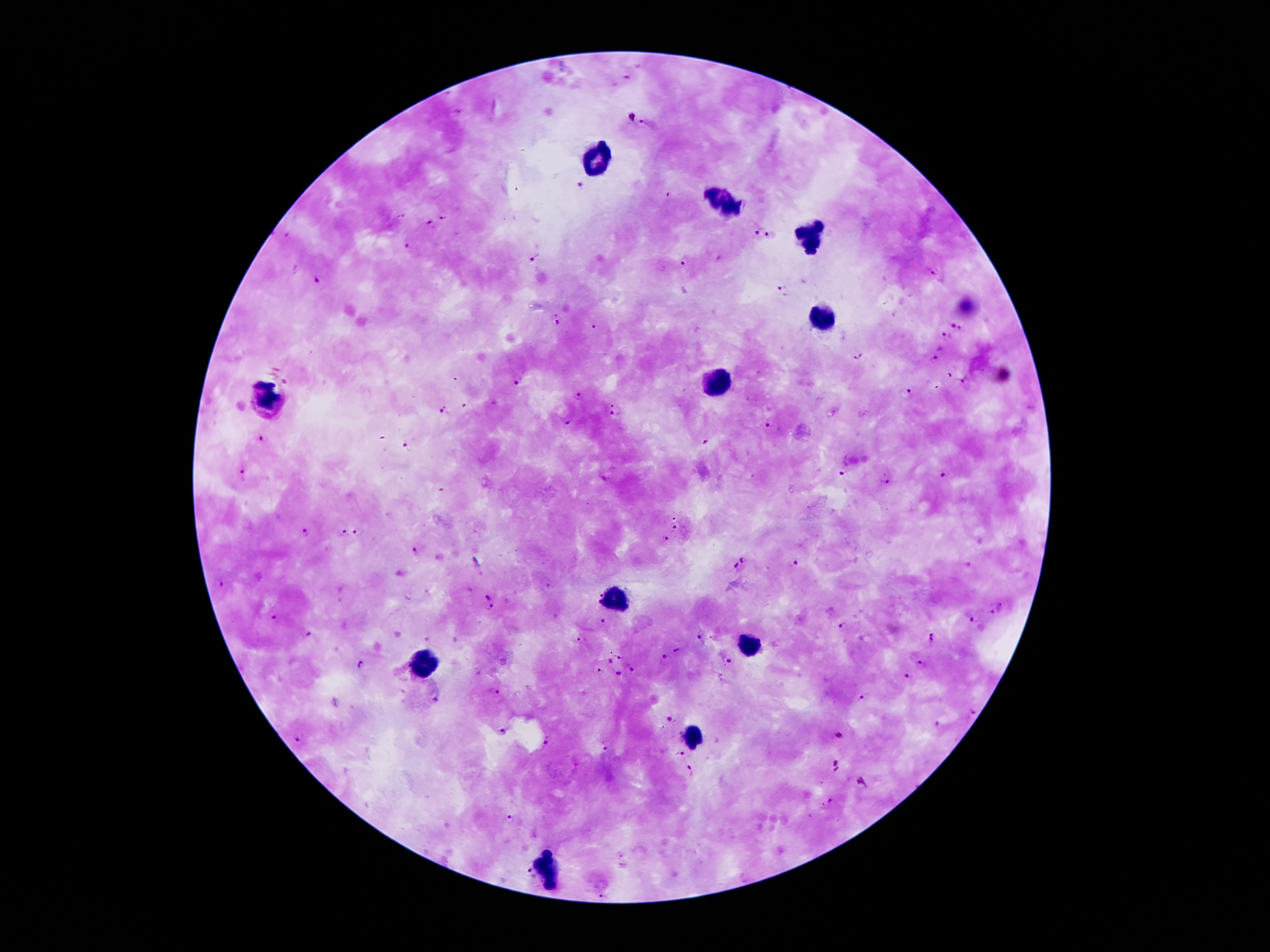
coordinate format = approximate object centers, in pixels from the top-left corner
Plasmodium parasite locations = (x=626, y=79), (x=646, y=124), (x=583, y=183), (x=670, y=194), (x=402, y=215), (x=445, y=215), (x=431, y=225), (x=760, y=231), (x=771, y=235), (x=289, y=236), (x=408, y=246), (x=534, y=258), (x=684, y=260), (x=933, y=272), (x=320, y=279), (x=783, y=290), (x=557, y=321), (x=596, y=327), (x=951, y=327), (x=960, y=330), (x=945, y=335), (x=860, y=355), (x=934, y=359), (x=950, y=376), (x=961, y=381), (x=518, y=382), (x=907, y=395), (x=579, y=397), (x=465, y=405), (x=445, y=409), (x=616, y=411), (x=569, y=421), (x=771, y=422), (x=264, y=438), (x=706, y=442), (x=406, y=445), (x=841, y=473), (x=942, y=473), (x=243, y=476), (x=886, y=478), (x=673, y=514), (x=675, y=527), (x=305, y=533), (x=343, y=533), (x=357, y=533), (x=664, y=539), (x=415, y=550), (x=744, y=558), (x=796, y=562), (x=737, y=568), (x=548, y=587), (x=600, y=594), (x=488, y=595), (x=597, y=602), (x=490, y=607), (x=275, y=616), (x=975, y=618), (x=601, y=622), (x=845, y=624), (x=307, y=628), (x=702, y=635), (x=583, y=638), (x=932, y=638), (x=677, y=649), (x=618, y=656), (x=665, y=657), (x=611, y=661), (x=728, y=661), (x=923, y=662), (x=362, y=665), (x=630, y=668), (x=598, y=669), (x=618, y=673), (x=905, y=680), (x=495, y=691), (x=863, y=698), (x=974, y=711), (x=671, y=718), (x=937, y=725), (x=502, y=729), (x=839, y=736), (x=299, y=738), (x=548, y=742), (x=605, y=745), (x=681, y=754), (x=688, y=770), (x=510, y=819), (x=527, y=870), (x=601, y=896)
leukocyte locations = (x=597, y=157), (x=721, y=201), (x=807, y=235), (x=817, y=319), (x=717, y=384), (x=267, y=398), (x=618, y=600), (x=746, y=642), (x=421, y=661), (x=693, y=737), (x=546, y=871)
magnification = 100x
preparation = thick blood smear
stain = Giemsa
capture = smartphone through the microscope eyepiece
image size = 1270×952 pixels
field of view = single
patient malaria status = positive for Plasmodium falciparum